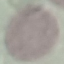
Summary:
  - Result: no malaria parasites seen
  - Stain: Giemsa
  - Image type: automatically extracted cell patch, resized to 64 × 64 pixels
  - Capture: smartphone through the microscope eyepiece
  - Preparation: thin blood film